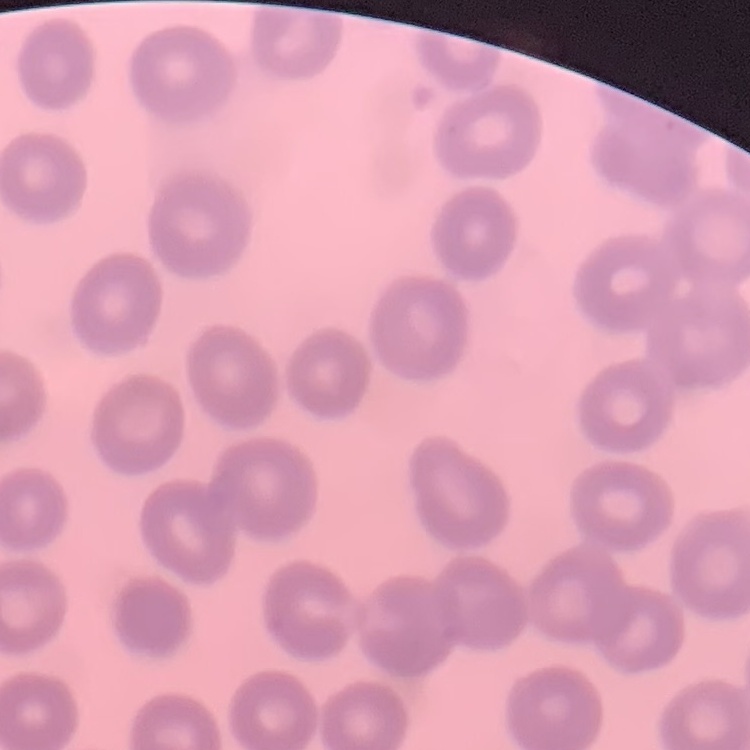
Summary:
  - Red blood cell morphology: no rouleaux formation
  - Stain: Field's or Giemsa
  - Image type: one tile cut from a larger photomicrograph
  - Preparation: thin peripheral smear